Comment on the morphology of the red blood cells.
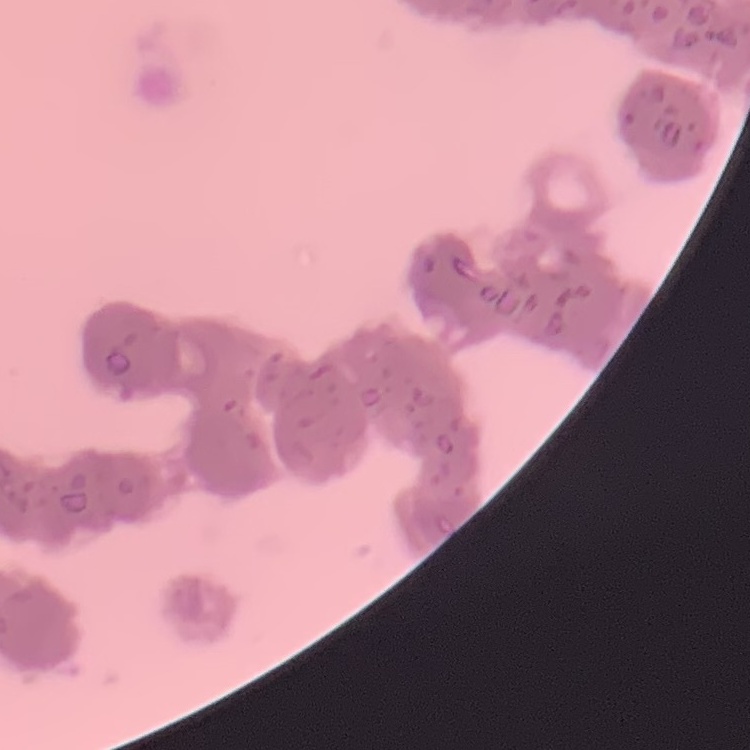
They show rouleaux formation.

Field's or Giemsa stain. Square crop of a larger photomicrograph. Thin peripheral smear.